State the preparation type.
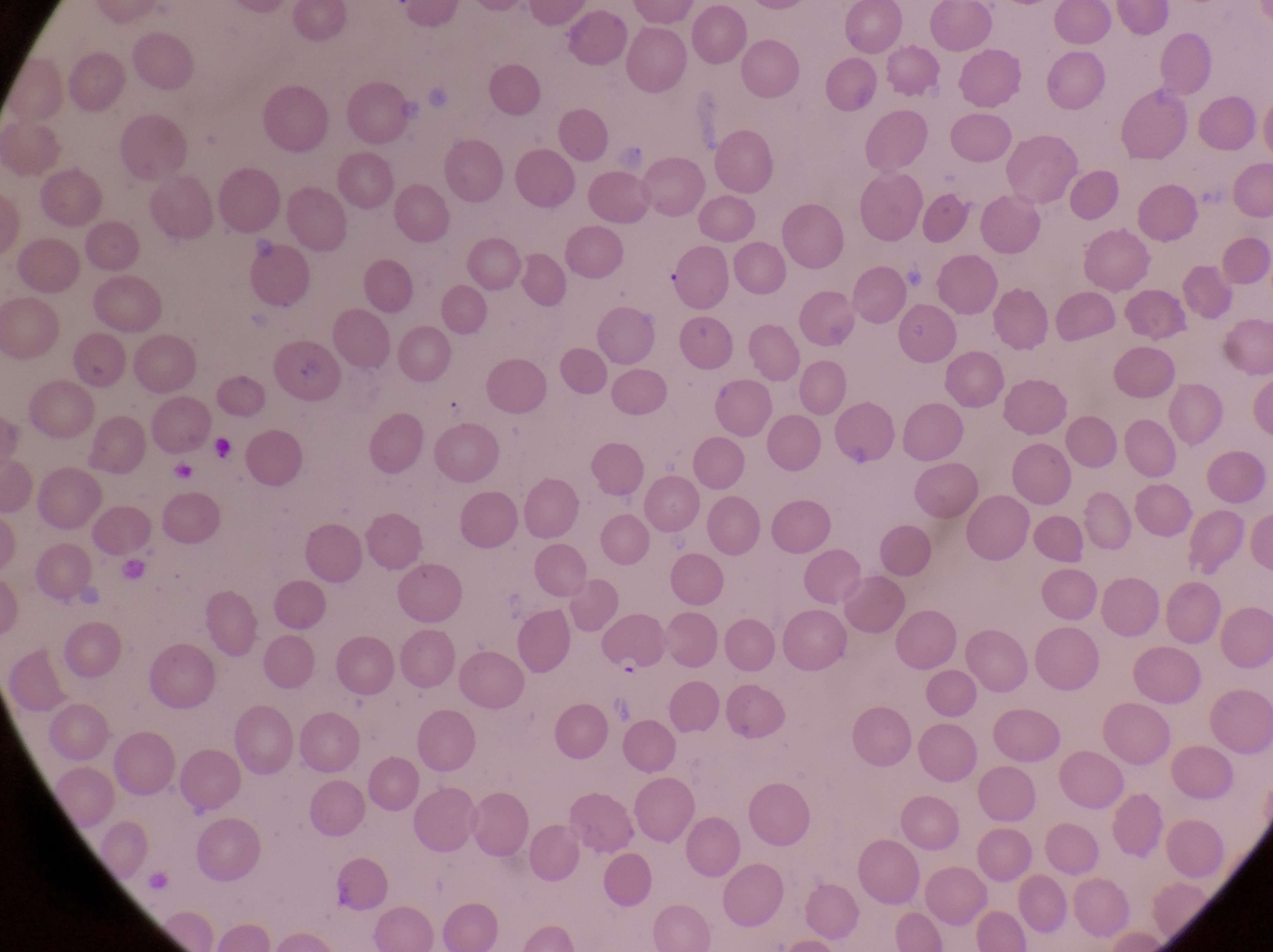

This is a thin smear.

Approximate bounding boxes as {left, top, right, bottom} in pixels. Parasitised red blood cell locations: {599, 617, 668, 679}. Single field of view. Image is 1273×952 pixels. Photographed through the eyepiece of an Olympus CX-23 microscope with a smartphone camera. Sample from Uganda. At a magnification of 1000x.